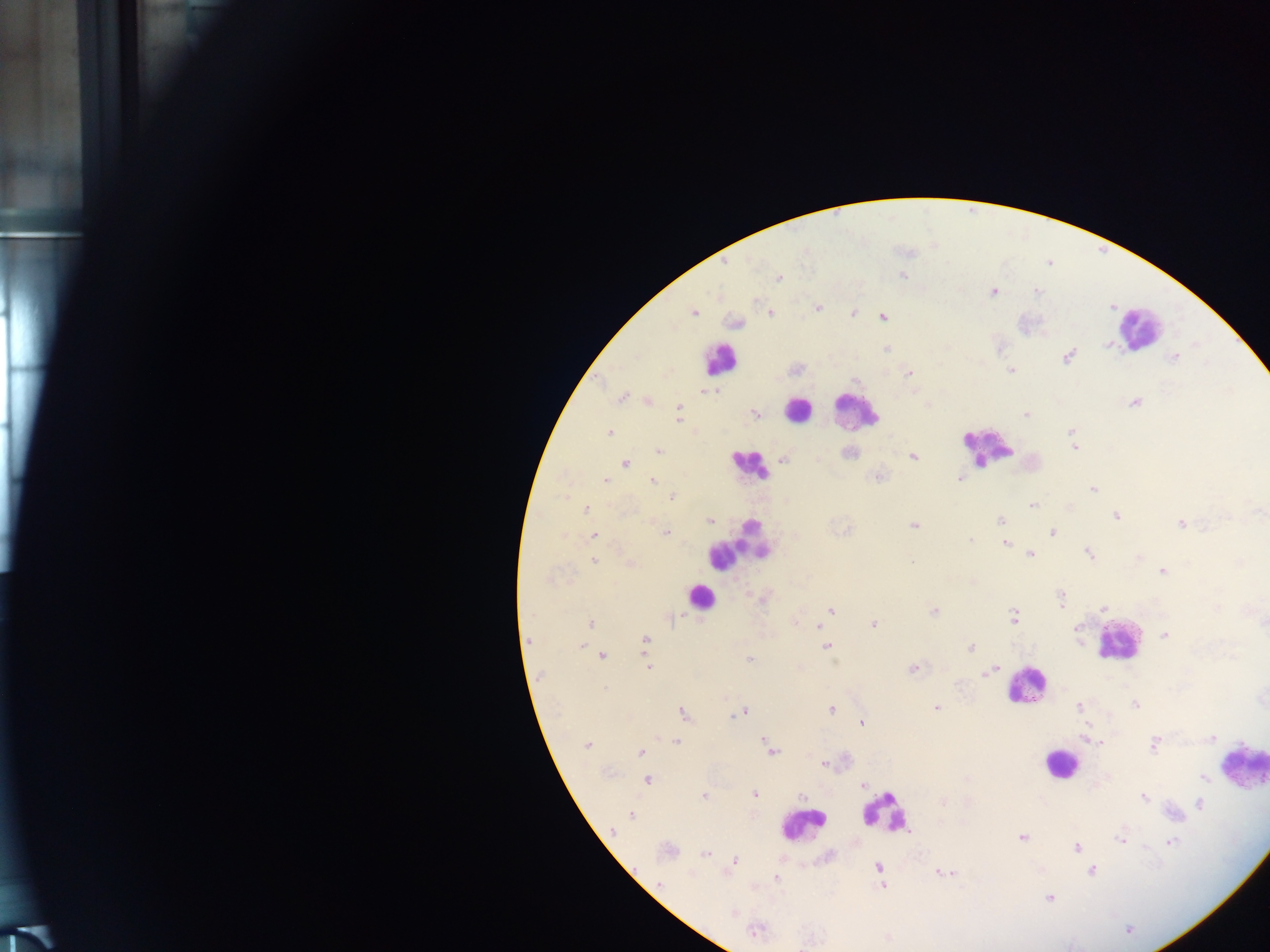

capture: mobile-phone photograph through a microscope
leukocyte_locations: 'approximate centers as (x, y) in pixels: (1139, 328), (720, 359), (798, 409), (855, 410), (988, 448), (748, 465), (737, 547), (699, 596), (1116, 640), (1025, 686), (1059, 764), (1243, 769), (885, 813), (801, 824)'
field_of_view: single
plasmodium_parasite_locations: 'approximate centers as (x, y) in pixels: (902, 275), (779, 278), (993, 292), (1037, 292), (818, 307), (694, 312), (853, 313), (771, 314), (883, 317), (734, 323), (1107, 345), (886, 349), (1067, 357), (1174, 357), (1011, 371), (909, 374), (714, 391), (708, 392), (621, 397), (649, 402), (1134, 403), (678, 407), (755, 413), (1025, 415), (678, 420), (1071, 432), (609, 433), (1074, 445), (659, 451), (849, 452), (913, 457), (784, 459), (626, 463), (877, 478), (960, 478), (605, 481), (652, 481), (1093, 489), (673, 497), (1031, 506), (586, 509), (1258, 511), (1115, 516), (1000, 521), (711, 522), (1181, 524), (913, 525), (1052, 532), (666, 533), (594, 536), (971, 540), (1005, 543), (1030, 554), (1089, 554), (1138, 557), (594, 561), (911, 561), (631, 564), (1162, 572), (548, 579), (1061, 599), (1104, 608), (831, 610), (934, 611), (1013, 616), (673, 618), (590, 623), (796, 623), (874, 624), (818, 626), (1164, 635), (646, 639), (581, 646), (826, 647), (970, 648), (603, 655), (748, 659), (648, 667), (912, 669), (991, 671), (1135, 705), (1080, 707), (831, 708), (936, 708), (743, 712), (683, 714), (861, 722), (1211, 738), (1088, 740), (765, 741), (677, 743), (587, 745), (1154, 745), (771, 751), (640, 752), (824, 763), (1202, 777), (648, 780), (863, 785), (755, 794), (703, 796), (802, 796), (1144, 797), (1200, 803), (631, 816), (613, 830), (1021, 838), (1120, 840), (1171, 842), (1076, 847), (667, 851), (705, 854), (736, 861), (878, 867), (1092, 871), (945, 872), (692, 874), (775, 878), (660, 884), (883, 886), (1048, 898), (733, 914), (755, 931)'
country: Ghana
image_size: 1270×952 pixels
preparation: thick blood film